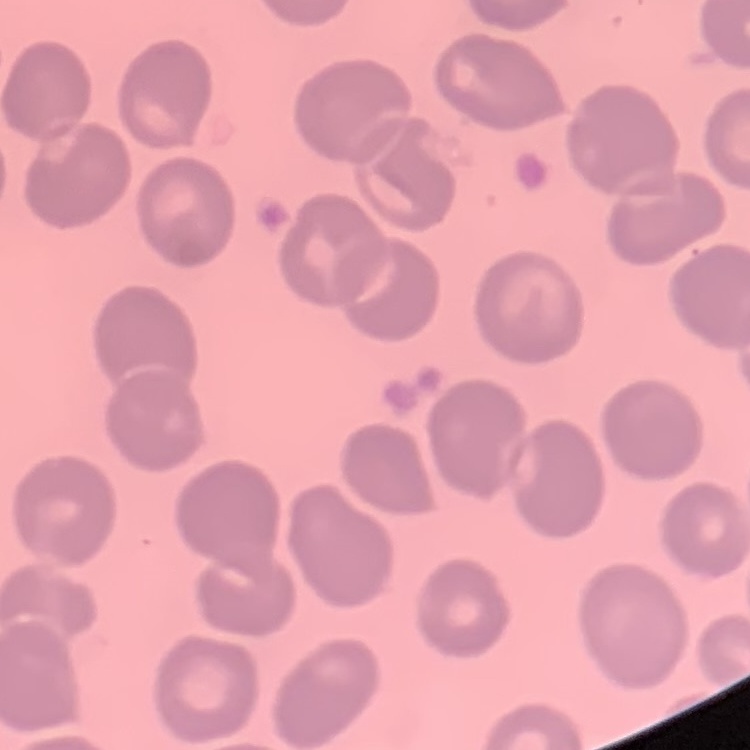 The erythrocytes exhibit no rouleaux formation. Square crop of a larger photomicrograph. Thin blood film. Field's or Giemsa stain.